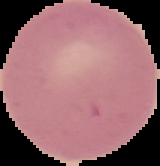

Summary:
  - Preparation: thin blood smear
  - Image size: 160×166 pixels
  - Image type: segmented cell region on a black background
  - Malaria status: uninfected